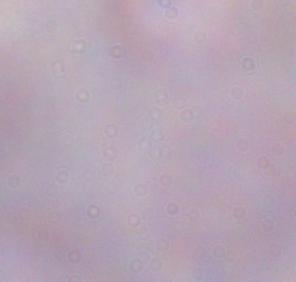

Summary:
  - Identification: trypanosome
  - Modality: micrograph
  - Magnification: 1000x